Assess this cell for malaria.
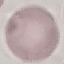
Uninfected.

Summary:
  - Stain: Giemsa
  - Image type: automatically extracted cell patch, resized to 64 × 64 pixels
  - Capture: smartphone through the microscope eyepiece
  - Preparation: thin smear